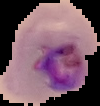

Summary:
  - Image size: 100×106 pixels
  - Image type: cell region segmented out of the field of view; surrounding area masked to black
  - Malaria status: parasitized
  - Preparation: thin blood smear